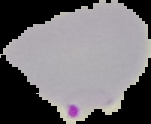

{
  "image_size": "151×124 pixels",
  "image_type": "segmented cell region on a black background",
  "malaria_status": "parasitized",
  "preparation": "thin blood film"
}